Look for Plasmodium parasites.
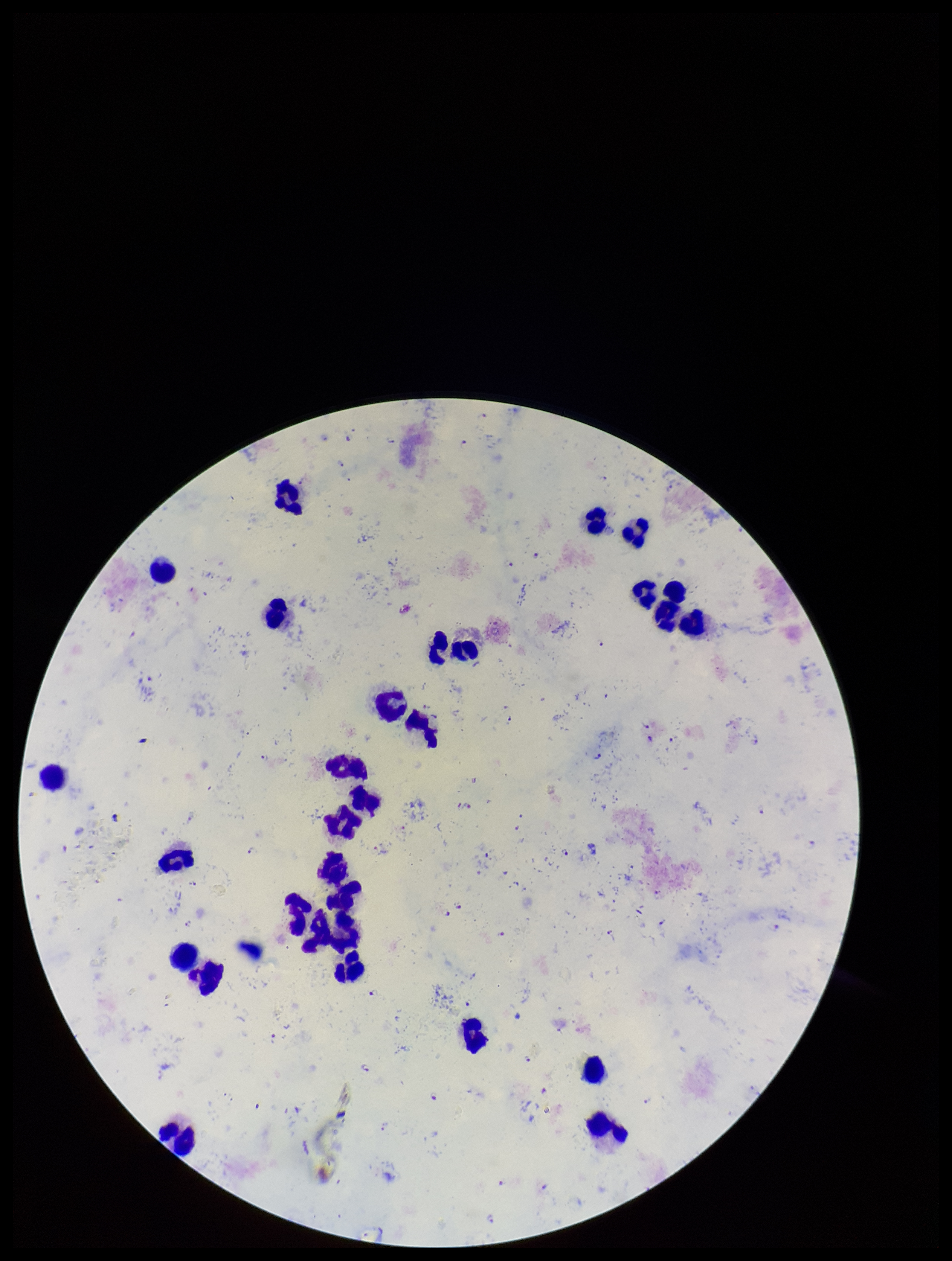
Detected.

Summary:
  - Patient malaria status: positive
  - Image size: 952×1261 pixels
  - Stain: Giemsa
  - Parasite count: 36
  - Field of view: one from this slide
  - Preparation: thick blood smear
  - Capture: smartphone photograph through the microscope eyepiece
  - Leukocyte count: 29
  - Species reported for this patient: Plasmodium falciparum